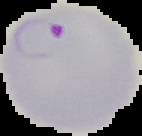
Summary:
  - Image size: 142×136 pixels
  - Result: Plasmodium parasites identified
  - Image type: segmented cell region with the area outside set to black
  - Preparation: thin blood film